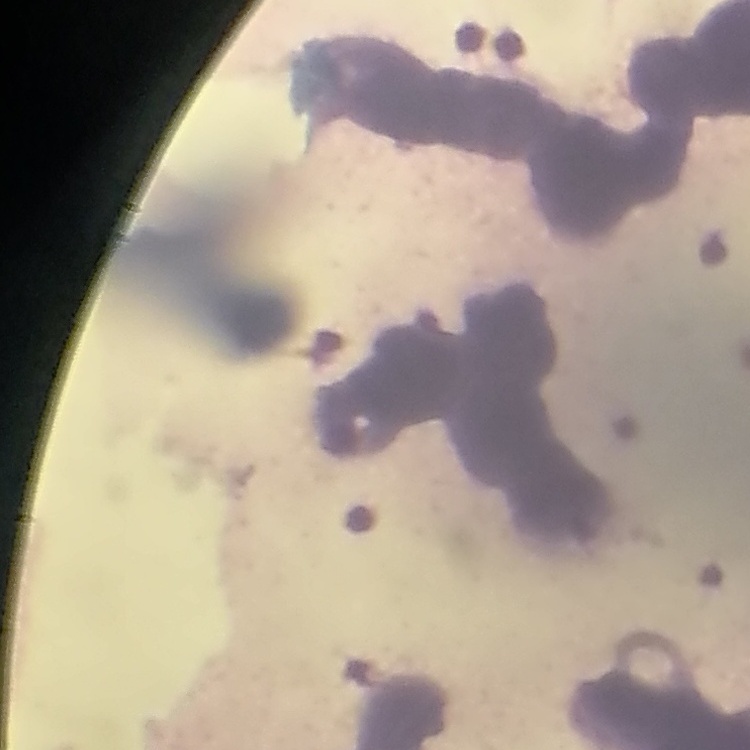 The red blood cells exhibit rouleaux formation. Stained with either Field's or Giemsa. Thin blood film. One tile cut from a larger photomicrograph.